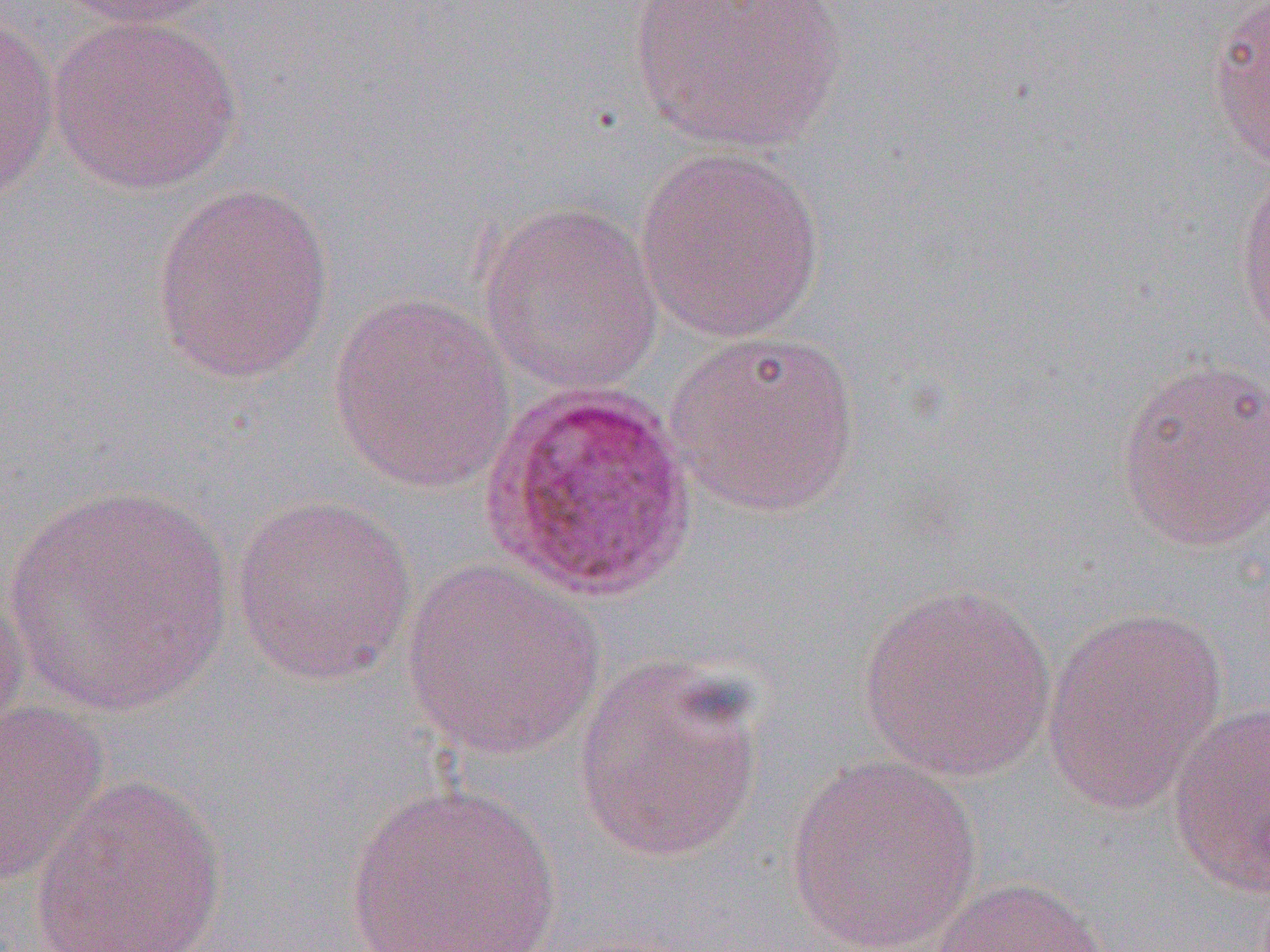 Approximate bounding boxes as (x1, y1, x2, y2) in pixels. Uninfected red blood cell locations: (55, 0, 227, 29), (628, 0, 848, 153), (1206, 1, 1270, 173), (0, 7, 60, 209), (49, 15, 243, 195), (632, 145, 828, 344), (1233, 162, 1270, 345), (151, 181, 335, 384), (474, 199, 664, 394), (327, 292, 517, 494), (666, 328, 863, 518), (1113, 357, 1270, 552), (4, 481, 236, 718), (230, 494, 418, 686), (400, 560, 607, 761), (0, 581, 31, 755), (857, 582, 1060, 782), (1042, 608, 1230, 815), (572, 653, 770, 864), (1167, 700, 1270, 898), (0, 701, 109, 890), (783, 754, 985, 952), (28, 774, 229, 952), (345, 781, 563, 950), (931, 875, 1113, 952). Plasmodium ovale-infected red blood cell locations: (479, 383, 698, 604). Slide-level diagnosis: Plasmodium ovale. Image is 1270×952 pixels. One field of a larger specimen. Thin blood smear. Optical microscopy. 1000x magnification.